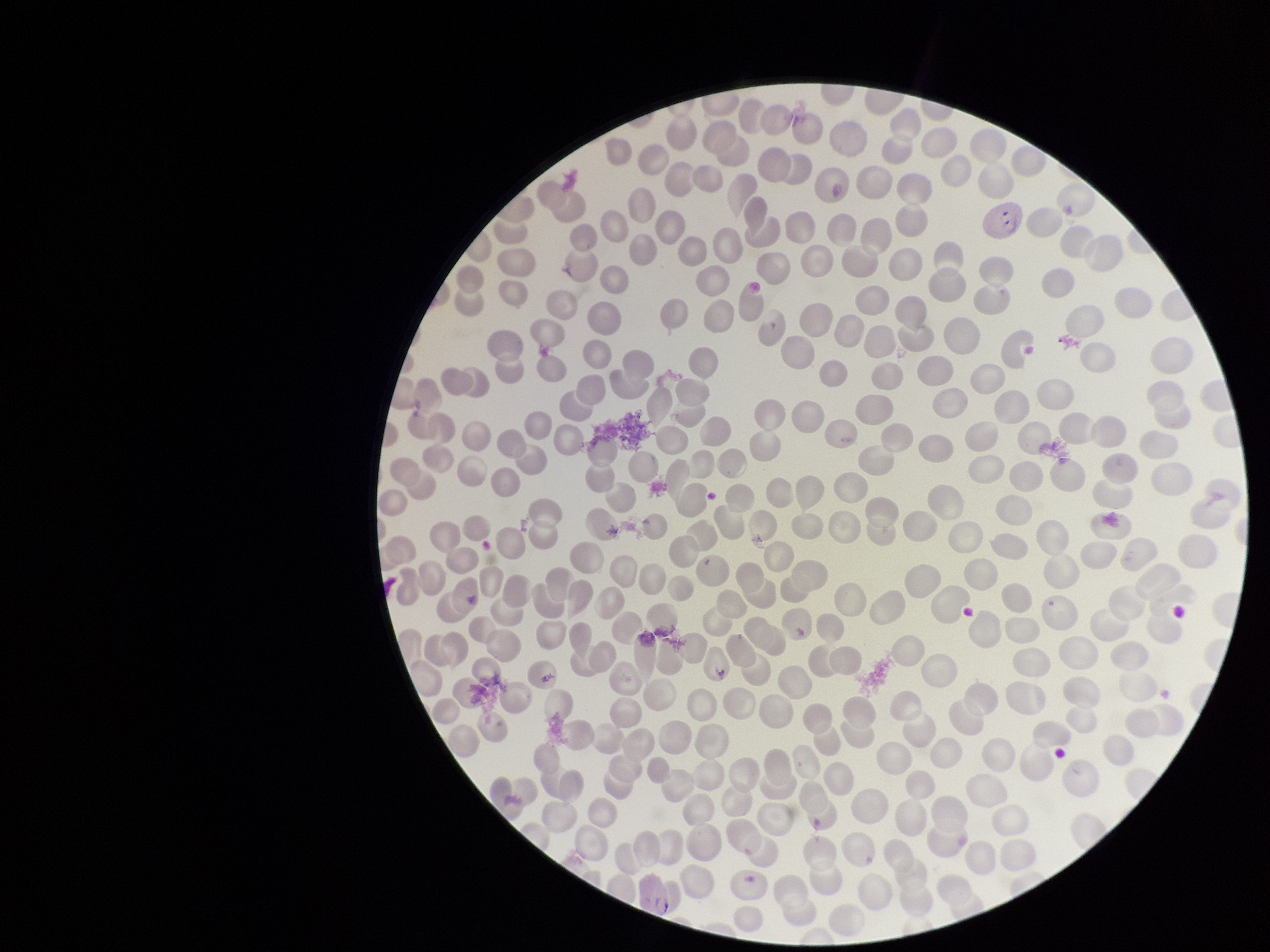

Summary:
  - Red blood cell count: 226
  - Parasitized red blood cell count: 2
  - Species reported for this patient: Plasmodium vivax
  - Patient malaria status: positive
  - Stain: Giemsa
  - Capture: smartphone photograph through the microscope eyepiece
  - Image size: 1270×952 pixels
  - Field of view: single
  - Parasitized red blood cells: detected
  - Preparation: thin blood smear